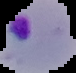
From a thin blood film. Malaria status: parasitized. Image is 76×73 pixels. Segmented cell region on a black background.